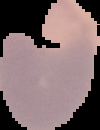
Image is 100×130 pixels. From a thin blood smear. Malaria status: parasitized. Cell region segmented out of the field of view; the surrounding area is masked to black.